Describe the morphology of the red blood cells.
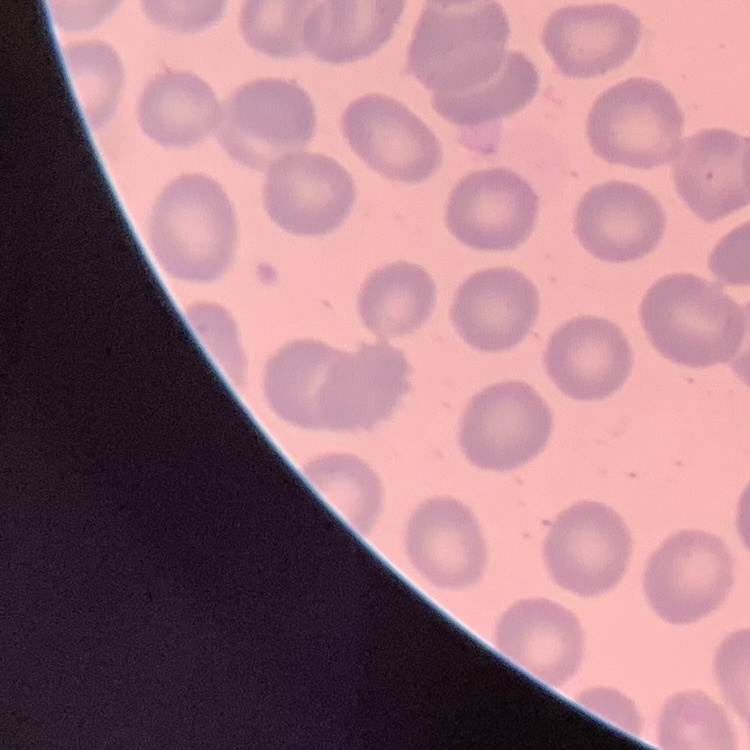
No rouleaux formation.

One tile cut from a larger photomicrograph. Thin peripheral smear. Field's or Giemsa stain.